State which cell type is depicted.
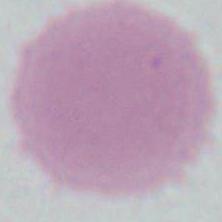

This is an erythrocyte.

modality = micrograph
magnification = 1000x